Name the cell type shown.
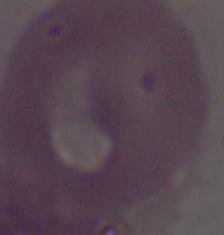
An erythrocyte.

{
  "modality": "photomicrograph",
  "magnification": "1000x"
}